Classify this cell by malaria status.
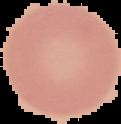

Uninfected.

From a thin blood smear. Image is 121×124 pixels. Cell region segmented out of the field of view; the surrounding area is masked to black.